Describe the morphology of the red blood cells.
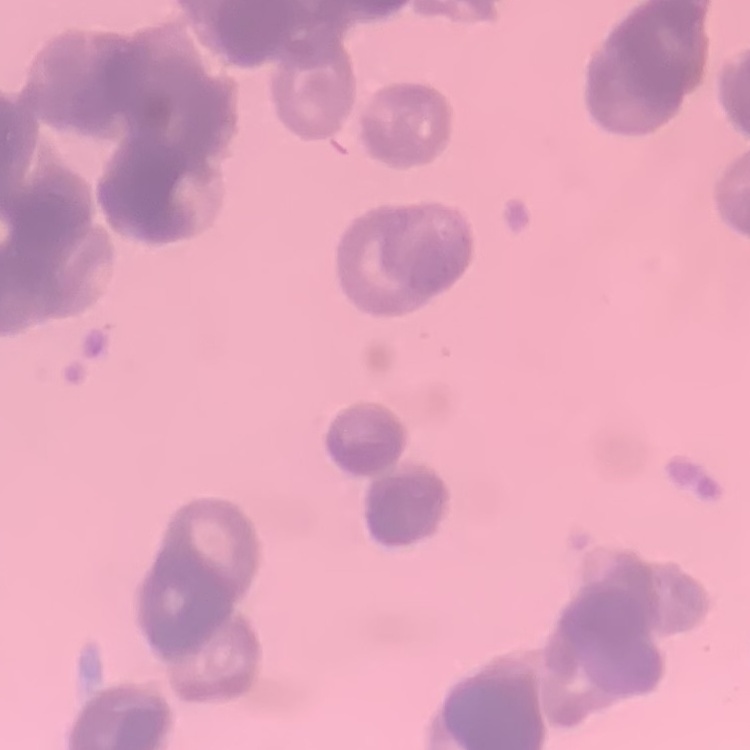
Rouleaux formation.

Field's or Giemsa stain. Thin blood film. One tile cut from a larger photomicrograph.